Identify the parasite.
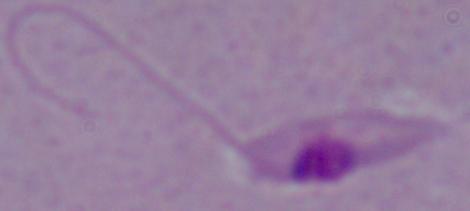

This is Leishmania.

Micrograph. Captured at 1000x magnification.